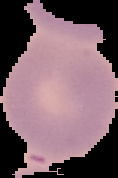
Summary:
  - Image size: 118×178 pixels
  - Malaria status: uninfected
  - Preparation: thin blood smear
  - Image type: segmented cell region on a black background